Comment on the morphology of the erythrocytes.
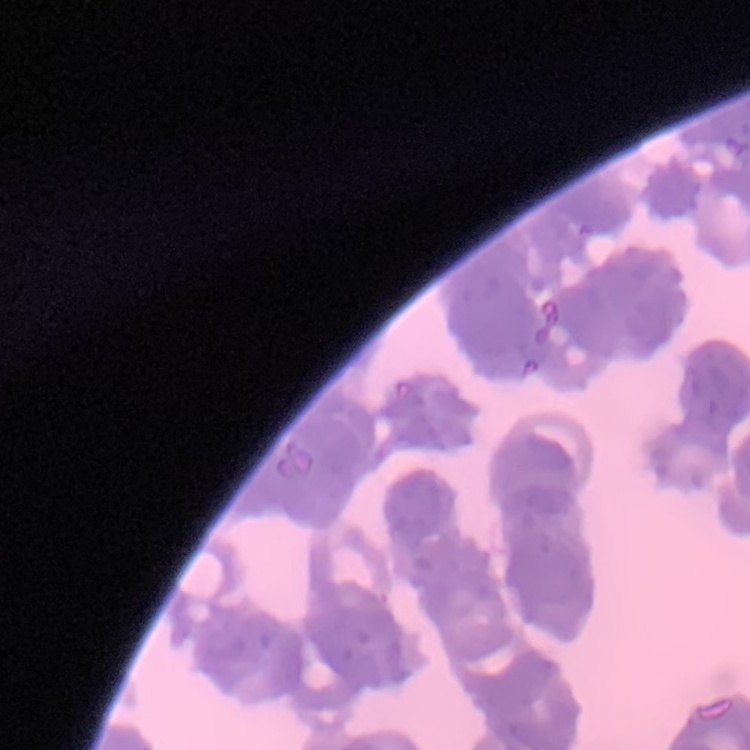
They show rouleaux formation.

Summary:
  - Image type: one tile cut from a larger photomicrograph
  - Stain: Field's or Giemsa
  - Preparation: thin blood smear